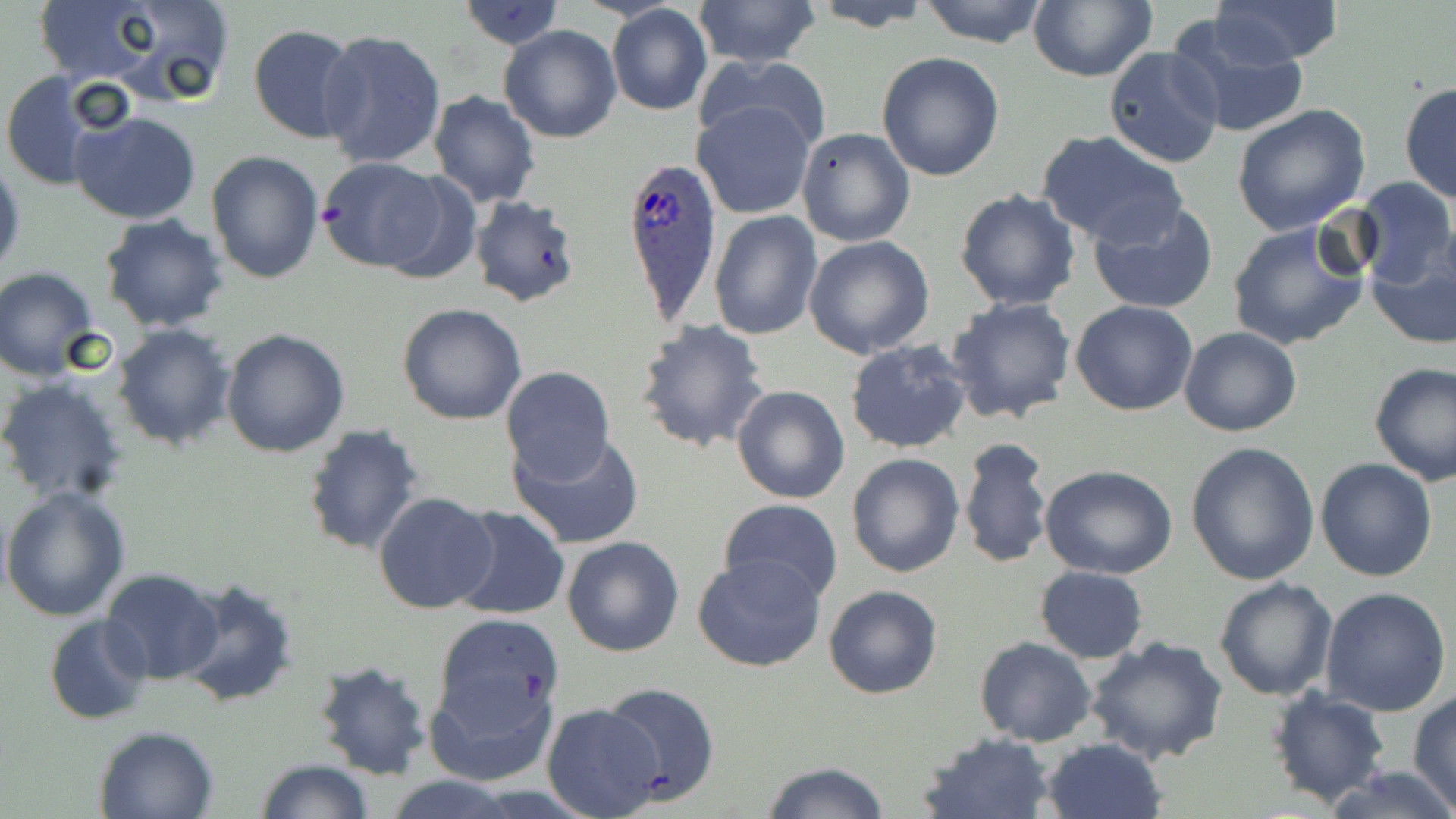

Approximate bounding boxes as (x1,y1)-(x2,y2) corner pairs in pixels. Plasmodium ovale-infected red blood cell locations: (619,153)-(720,325). Uninfected red blood cell locations: (26,0)-(176,88), (90,0)-(237,106), (691,0)-(821,70), (917,0)-(1049,47), (1028,0)-(1156,82), (1211,0)-(1342,65), (459,1)-(563,51), (804,1)-(936,32), (607,5)-(713,117), (1167,13)-(1309,142), (248,24)-(361,143), (499,24)-(622,143), (318,28)-(447,170), (1103,46)-(1225,170), (876,52)-(1005,181), (696,53)-(834,158), (0,72)-(106,192), (1399,81)-(1456,205), (428,91)-(541,207), (693,99)-(817,218), (1231,103)-(1371,235), (71,109)-(202,225), (796,127)-(916,248), (1037,129)-(1188,247), (206,149)-(324,284), (0,156)-(25,280), (315,158)-(452,273), (1351,176)-(1455,287), (954,188)-(1081,311), (468,194)-(583,309), (1086,199)-(1219,316), (710,210)-(823,341), (99,214)-(230,333), (1226,218)-(1372,351), (803,235)-(934,359), (1366,248)-(1456,349), (1,268)-(101,380), (946,297)-(1077,424), (1071,301)-(1199,417), (396,302)-(528,426), (635,318)-(770,454), (112,323)-(237,450), (1179,327)-(1303,437), (221,329)-(350,459), (843,338)-(972,455), (1368,360)-(1456,484), (498,365)-(615,486), (0,376)-(129,506), (731,384)-(850,505), (302,424)-(424,558), (508,431)-(646,550), (958,437)-(1053,570), (1186,441)-(1320,584), (846,452)-(964,577), (1315,458)-(1438,582), (1039,463)-(1178,579), (1,487)-(130,621), (372,489)-(497,615), (719,499)-(843,604), (448,506)-(570,621), (562,535)-(686,658), (692,553)-(826,673), (1035,566)-(1148,662), (100,568)-(226,685), (174,576)-(300,709), (1213,577)-(1338,701), (823,584)-(943,698), (1320,587)-(1452,717), (43,614)-(152,726), (432,614)-(564,749), (1083,636)-(1229,765), (975,637)-(1097,747), (312,658)-(434,781), (425,665)-(557,787), (600,681)-(720,804), (1266,688)-(1391,807), (1408,692)-(1456,810), (540,703)-(664,817), (93,724)-(220,818), (917,732)-(1056,818), (1040,737)-(1166,819), (253,759)-(373,818), (759,761)-(892,819), (1325,764)-(1456,819), (384,775)-(522,818). Slide-level diagnosis: Plasmodium ovale. May-Grünwald-Giemsa stain. Single field of view. Image is 1456×819 pixels. Light microscopy. Thin blood smear. Captured at 1000x magnification.